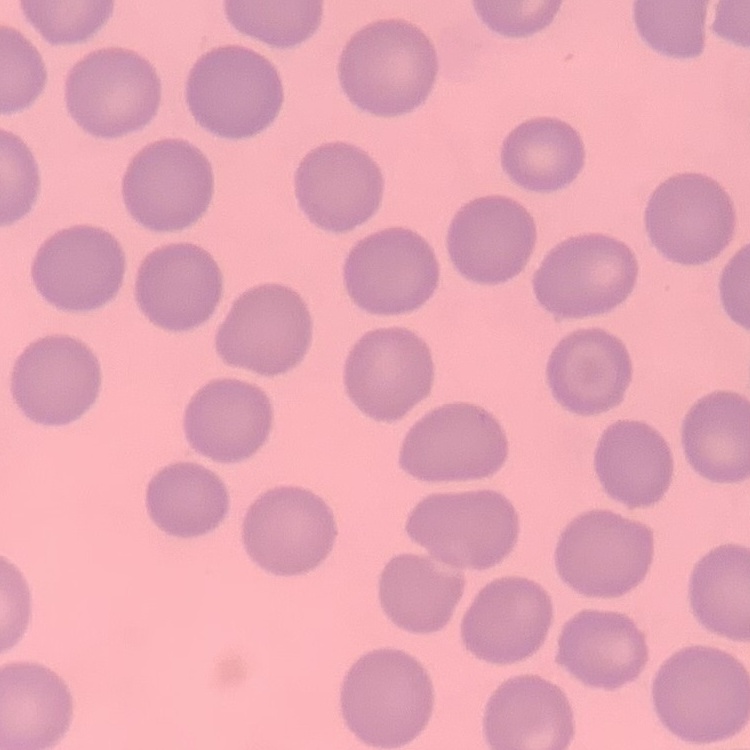

erythrocyte morphology = no rouleaux formation
image type = one tile cut from a larger photomicrograph
preparation = thin blood film
stain = Field's or Giemsa